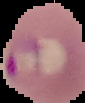
Summary:
  - Image size: 85×103 pixels
  - Preparation: thin blood smear
  - Image type: segmented cell region with the area outside set to black
  - Malaria status: parasitized